Name the parasite shown.
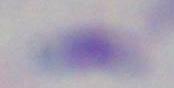

This is Toxoplasma gondii.

magnification: 1000x
modality: photomicrograph